Give the position of every malaria parasite.
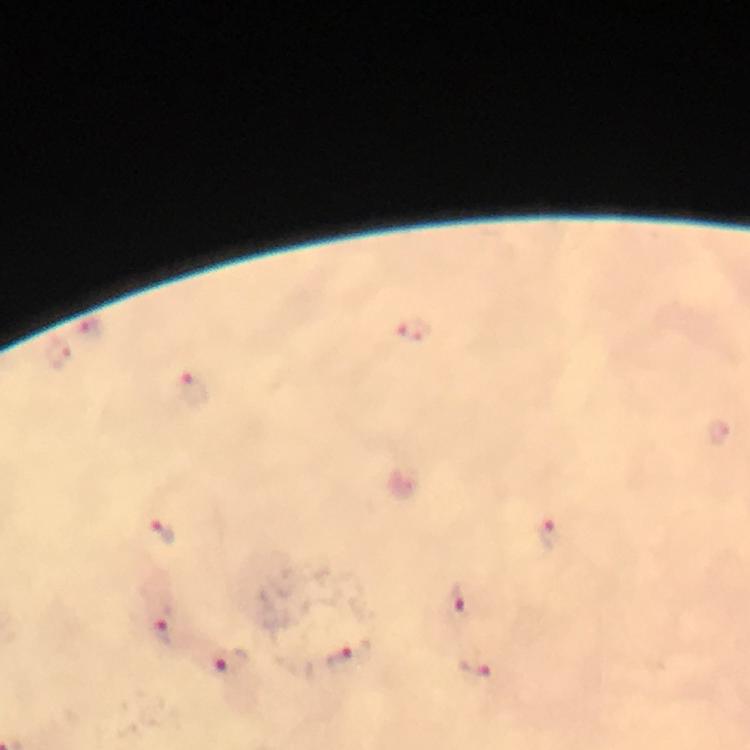
Approximate centers as {x, y} in pixels.
Malaria parasites: {90, 326}, {416, 329}, {57, 352}, {195, 390}, {162, 531}, {548, 532}, {456, 601}, {164, 631}, {348, 656}, {228, 661}, {476, 664}.

magnification = 100x
stain = Giemsa
cropped from = a single field of view
immersion oil = applied
image size = 750×750 pixels
preparation = thick smear
capture = smartphone photograph through a microscope
context = from a diagnostic examination for malaria